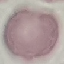

result = negative for malaria parasites
capture = smartphone camera at the microscope eyepiece
preparation = thin blood smear
stain = Giemsa
image type = automatically extracted cell patch, resized to 64 × 64 pixels